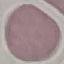

Summary:
  - Malaria status: uninfected
  - Stain: Giemsa
  - Capture: smartphone camera at the microscope eyepiece
  - Preparation: thin blood film
  - Image type: cell patch, automatically extracted from a larger field of view and resized to 64 × 64 pixels